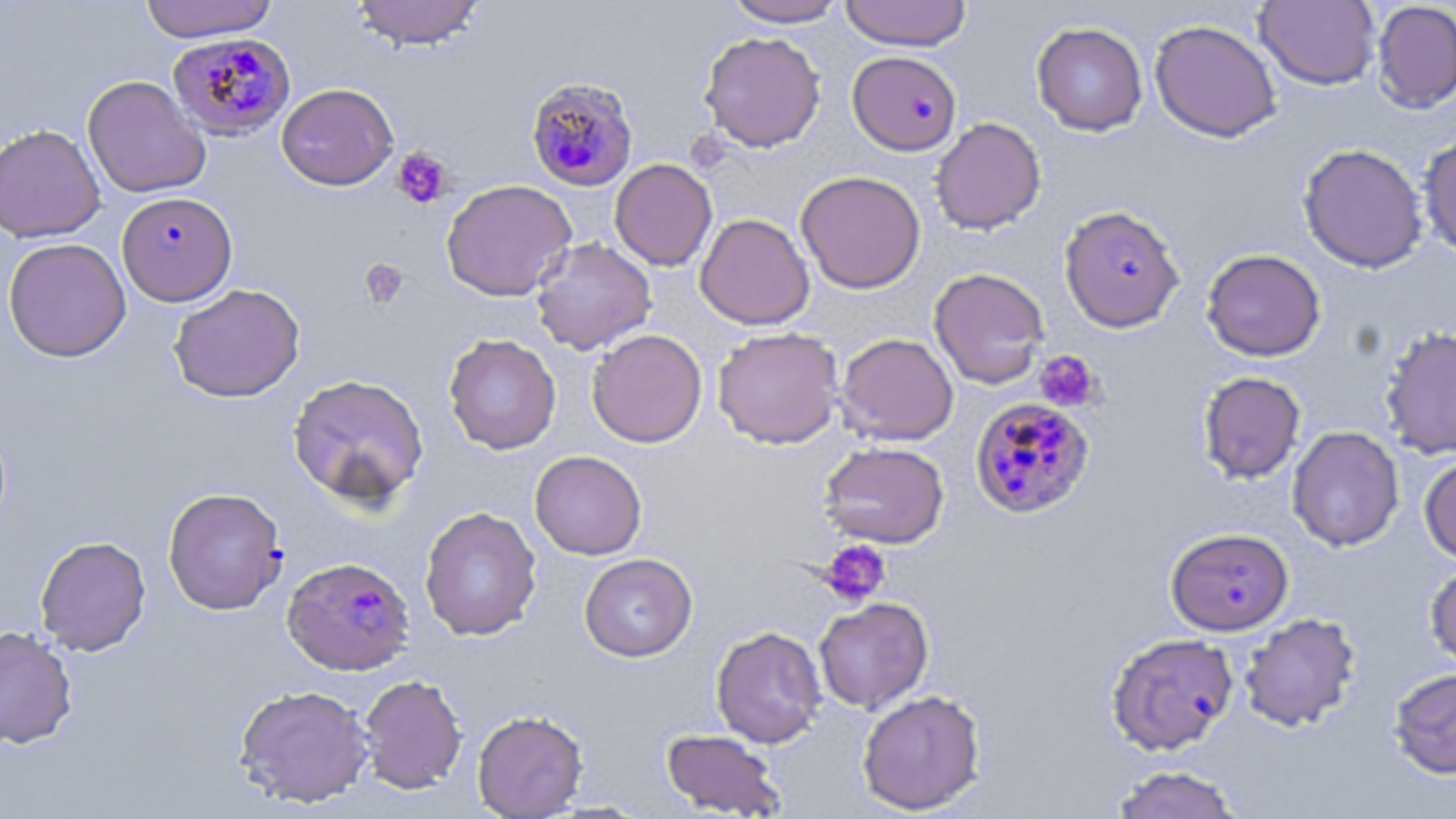
Summary:
  - Coordinate format: approximate bounding boxes as (x1, y1, x2, y2) in pixels
  - Plasmodium falciparum-infected red blood cell locations: (166, 32, 297, 141), (846, 54, 960, 158), (524, 72, 640, 187), (117, 191, 237, 306), (1058, 204, 1185, 332), (972, 394, 1098, 517), (163, 486, 288, 615), (1165, 526, 1294, 635), (282, 557, 414, 676), (1105, 632, 1239, 756)
  - Platelet locations: (391, 147, 454, 209), (359, 258, 410, 309), (1034, 350, 1101, 412), (818, 540, 891, 608)
  - Uninfected red blood cell locations: (139, 0, 278, 42), (351, 0, 486, 50), (723, 0, 848, 27), (839, 0, 973, 51), (1255, 0, 1380, 90), (1371, 1, 1456, 113), (1149, 19, 1282, 143), (1031, 21, 1148, 136), (699, 31, 826, 152), (82, 75, 210, 198), (276, 82, 399, 190), (930, 117, 1046, 235), (0, 123, 105, 243), (1418, 130, 1456, 260), (1297, 142, 1429, 273), (609, 158, 718, 271), (795, 170, 926, 294), (441, 179, 577, 302), (695, 212, 814, 330), (2, 237, 132, 362), (530, 237, 657, 355), (1200, 248, 1313, 485), (1201, 248, 1326, 361), (929, 267, 1050, 389), (168, 283, 305, 403), (1379, 325, 1456, 459), (712, 327, 844, 449), (587, 329, 707, 448), (835, 332, 958, 445), (443, 333, 561, 454), (1198, 371, 1306, 484), (287, 373, 430, 509), (1287, 426, 1404, 552), (818, 441, 950, 548), (529, 450, 647, 560), (1419, 454, 1456, 563), (419, 506, 542, 641), (34, 535, 151, 656), (579, 553, 697, 662), (1424, 561, 1456, 672), (814, 597, 934, 714), (1239, 612, 1362, 732), (0, 624, 79, 749), (711, 625, 827, 748), (1388, 668, 1456, 779), (358, 674, 467, 794), (233, 683, 374, 808), (857, 689, 987, 814), (472, 709, 589, 818), (660, 729, 788, 817), (1110, 764, 1244, 819)
  - Slide-level diagnosis: Plasmodium falciparum
  - Magnification: 1000x
  - Field of view: one of a larger specimen
  - Stain: May-Grünwald-Giemsa
  - Modality: optical microscopy
  - Image size: 1456×819 pixels
  - Preparation: thin blood smear